Give the position of every leukocyte visible.
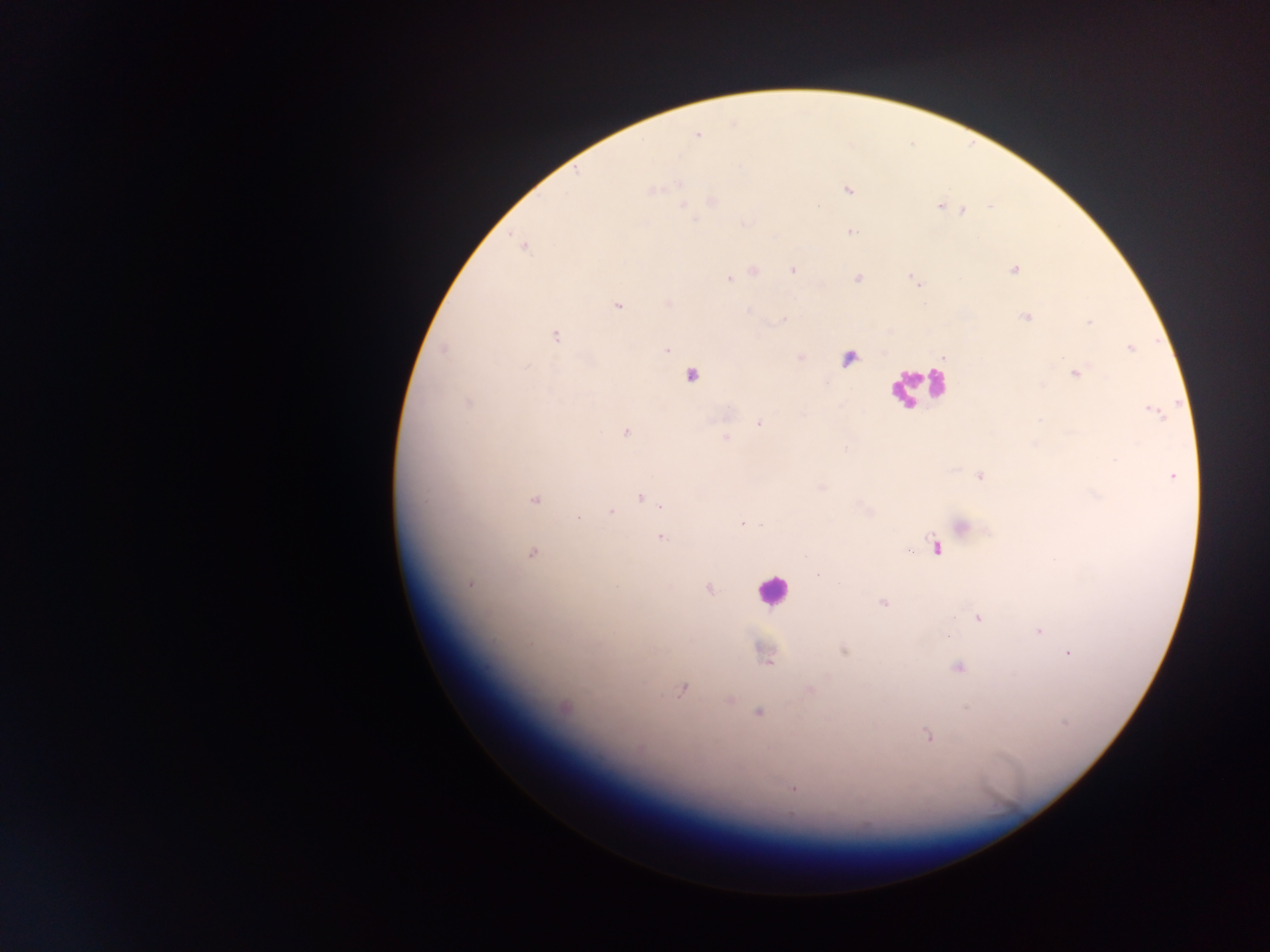

Approximate centers as [x, y] in pixels.
Leukocytes: [915, 385], [771, 590].

Summary:
  - Malaria parasite locations: [697, 135], [653, 190], [848, 190], [713, 202], [938, 206], [684, 207], [963, 211], [851, 231], [524, 246], [793, 270], [1014, 270], [753, 271], [858, 278], [729, 279], [618, 305], [749, 311], [1027, 317], [783, 319], [1089, 322], [556, 336], [1130, 349], [442, 350], [667, 350], [801, 357], [527, 366], [1077, 373], [691, 376], [468, 402], [1155, 412], [759, 423], [625, 433], [726, 438], [981, 476], [1173, 477], [640, 498], [535, 500], [662, 506], [610, 512], [578, 518], [742, 524], [962, 526], [662, 538], [935, 547], [908, 551], [532, 553], [469, 585], [708, 589], [884, 604], [978, 619], [1039, 631], [844, 650], [1068, 653], [766, 657], [957, 668], [682, 689], [810, 690], [730, 700], [563, 708], [759, 712], [1064, 723], [928, 735], [793, 788]
  - Preparation: thick blood film
  - Image size: 1270×952 pixels
  - Country: Ghana
  - Field of view: single
  - Capture: mobile-phone photograph through a microscope